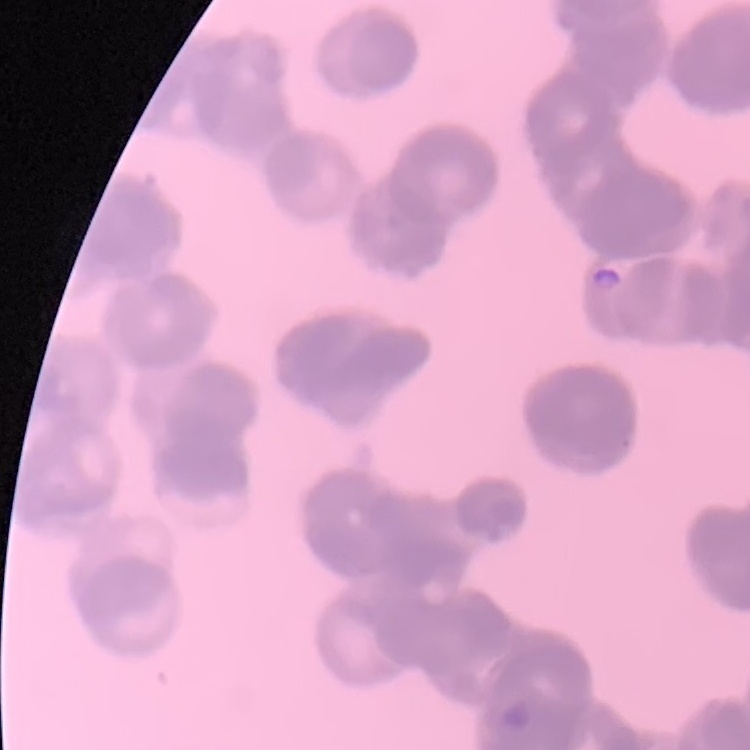
red blood cell morphology = rouleaux formation
stain = Field's or Giemsa
preparation = thin blood smear
image type = square crop of a larger photomicrograph